Assess for malaria.
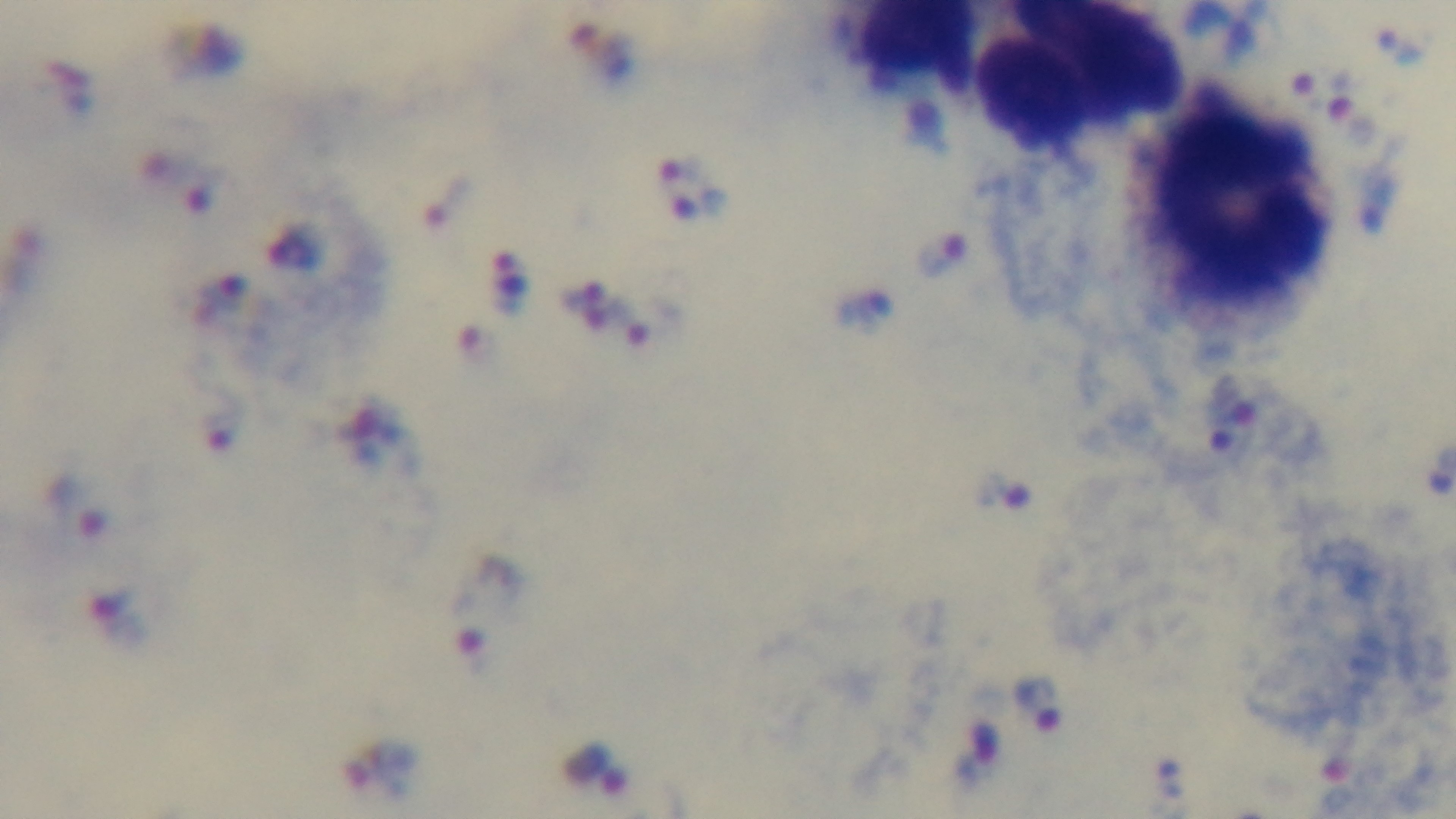
Infected.

Captured with a mounted 4K digital camera. 100x oil-immersion objective. Single field of view. Preparation: thick blood film. Light microscopy. Giemsa-stained.